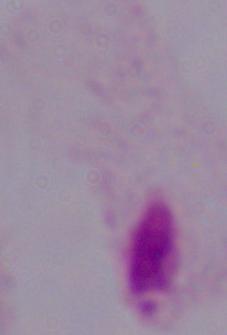

Captured at 1000x magnification. A trichomonad is shown. Photomicrograph.